Mark where cells are.
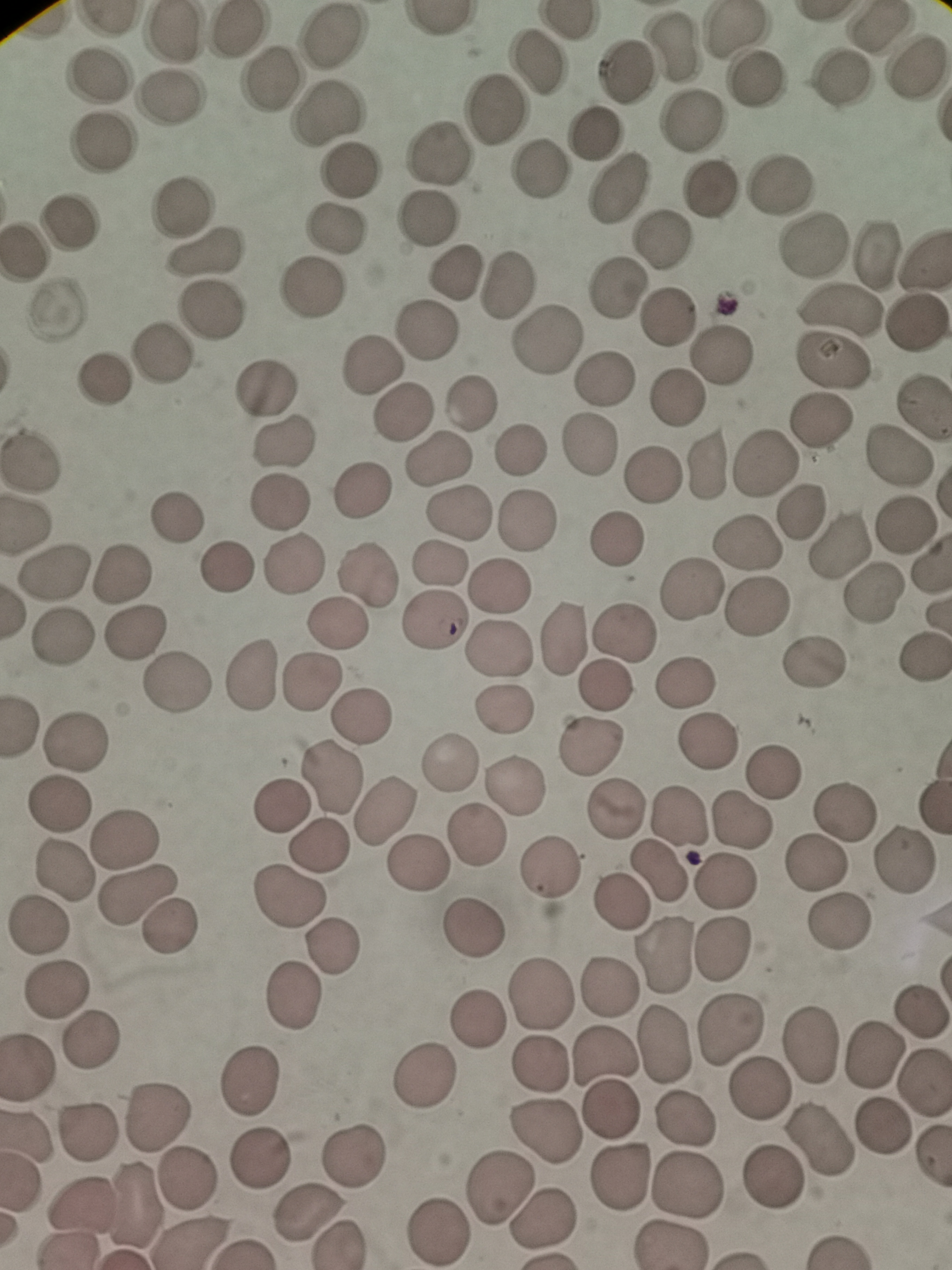

Approximate centers as {x, y} in pixels.
Cells: {877, 25}, {175, 32}, {234, 32}, {738, 32}, {332, 40}, {676, 47}, {536, 59}, {917, 67}, {266, 75}, {623, 75}, {99, 76}, {841, 78}, {757, 86}, {168, 97}, {493, 109}, {324, 117}, {693, 120}, {594, 135}, {101, 144}, {435, 152}, {540, 169}, {349, 171}, {781, 183}, {618, 189}, {711, 191}, {183, 204}, {430, 217}, {71, 222}, {335, 231}, {658, 240}, {816, 244}, {879, 251}, {23, 252}, {204, 254}, {455, 271}, {506, 283}, {312, 287}, {615, 288}, {840, 310}, {213, 312}, {667, 312}, {916, 319}, {428, 332}, {541, 343}, {161, 350}, {723, 350}, {372, 365}, {830, 366}, {104, 379}, {606, 379}, {264, 388}, {676, 398}, {471, 404}, {924, 405}, {404, 411}, {823, 422}, {283, 444}, {589, 445}, {517, 451}, {897, 457}, {31, 458}, {438, 458}, {704, 465}, {766, 465}, {652, 473}, {360, 493}, {282, 503}, {800, 511}, {459, 516}, {173, 518}, {526, 521}, {904, 525}, {615, 540}, {747, 542}, {837, 544}, {295, 563}, {438, 564}, {227, 569}, {53, 572}, {123, 574}, {368, 575}, {503, 587}, {691, 594}, {874, 595}, {759, 608}, {435, 620}, {337, 624}, {137, 630}, {624, 632}, {565, 636}, {62, 640}, {500, 647}, {923, 657}, {813, 662}, {250, 676}, {312, 679}, {689, 682}, {177, 683}, {605, 685}, {504, 712}, {360, 717}, {77, 742}, {708, 743}, {589, 745}, {451, 763}, {772, 769}, {329, 777}, {518, 786}, {59, 805}, {282, 805}, {616, 805}, {844, 811}, {383, 813}, {681, 817}, {740, 820}, {474, 835}, {125, 838}, {319, 844}, {904, 859}, {815, 863}, {420, 864}, {551, 867}, {63, 872}, {661, 873}, {727, 884}, {136, 894}, {288, 898}, {621, 905}, {837, 920}, {37, 929}, {173, 931}, {474, 933}, {723, 948}, {336, 950}, {661, 957}, {58, 985}, {607, 985}, {540, 993}, {296, 997}, {919, 1013}, {478, 1019}, {732, 1029}, {93, 1038}, {667, 1041}, {811, 1047}, {872, 1052}, {604, 1055}, {541, 1063}, {28, 1068}, {426, 1077}, {252, 1080}, {923, 1084}, {760, 1089}, {613, 1110}, {157, 1111}, {683, 1119}, {547, 1130}, {883, 1132}, {89, 1135}, {822, 1148}, {354, 1152}, {256, 1156}, {620, 1177}, {186, 1178}, {773, 1178}, {694, 1185}, {498, 1188}, {134, 1202}, {80, 1204}, {310, 1216}, {548, 1219}, {442, 1228}.

Image is 952×1270 pixels. One field from this slide. Giemsa stain. Thin blood smear. Photographed with a smartphone camera at the microscope eyepiece.